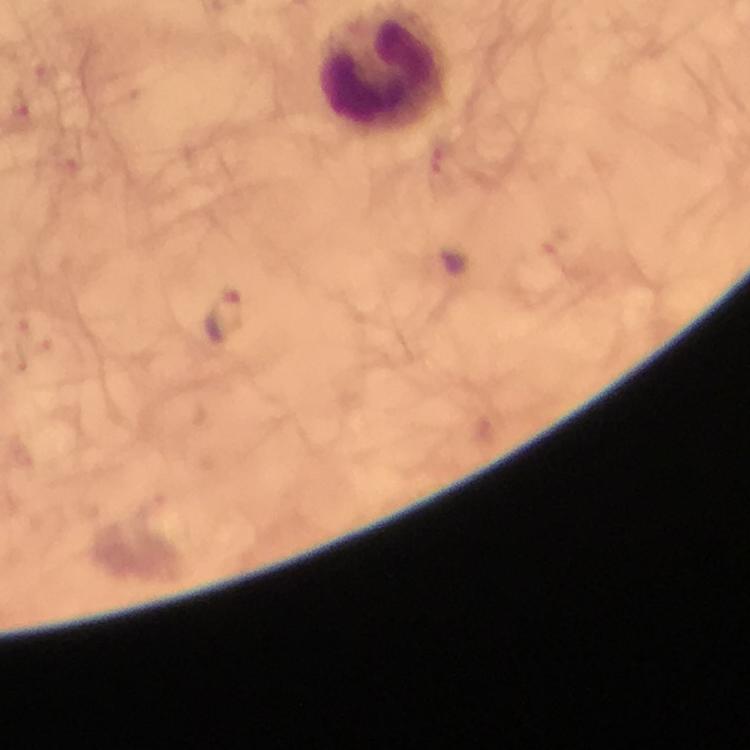

Approximate object centers, in pixels from the top-left corner. Plasmodium parasite locations: (x=46, y=74), (x=20, y=101), (x=442, y=158), (x=225, y=316), (x=20, y=323), (x=43, y=344). Leukocyte locations: (x=381, y=66). A crop from one field of view. Thick blood film. Immersion oil applied. From a diagnostic examination for malaria. Photographed through the microscope with a smartphone camera. Image is 750×750 pixels. At 100x magnification. Giemsa-stained preparation.